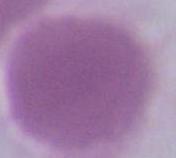
{
  "identification": "red blood cell",
  "modality": "micrograph",
  "magnification": "1000x"
}